Locate every Plasmodium parasite.
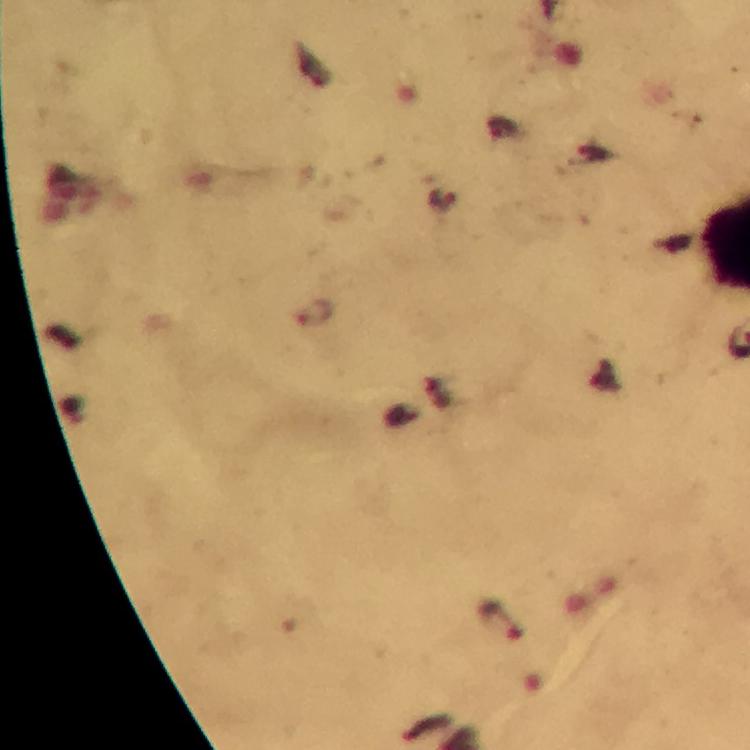

Approximate object centers, in pixels from the top-left corner.
Plasmodium parasites: (x=313, y=314), (x=501, y=620).

Immersion oil applied. Giemsa-stained preparation. Thick smear. From a malaria diagnostic workup. A crop from one field of view. Image is 750×750 pixels. Smartphone photograph taken through a microscope. 100x magnification.